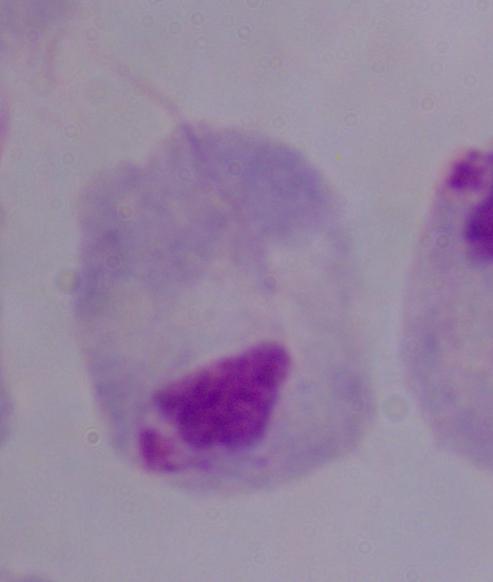
Micrograph. Captured at 1000x magnification. A trichomonad is seen.